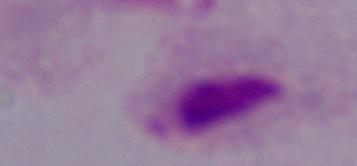
Summary:
  - Magnification: 1000x
  - Modality: photomicrograph
  - Identification: trichomonad